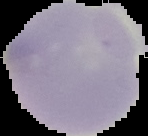

image size = 148×136 pixels
image type = segmented cell region on a black background
malaria status = uninfected
preparation = thin blood film